Outline each blood parasite and name the species.
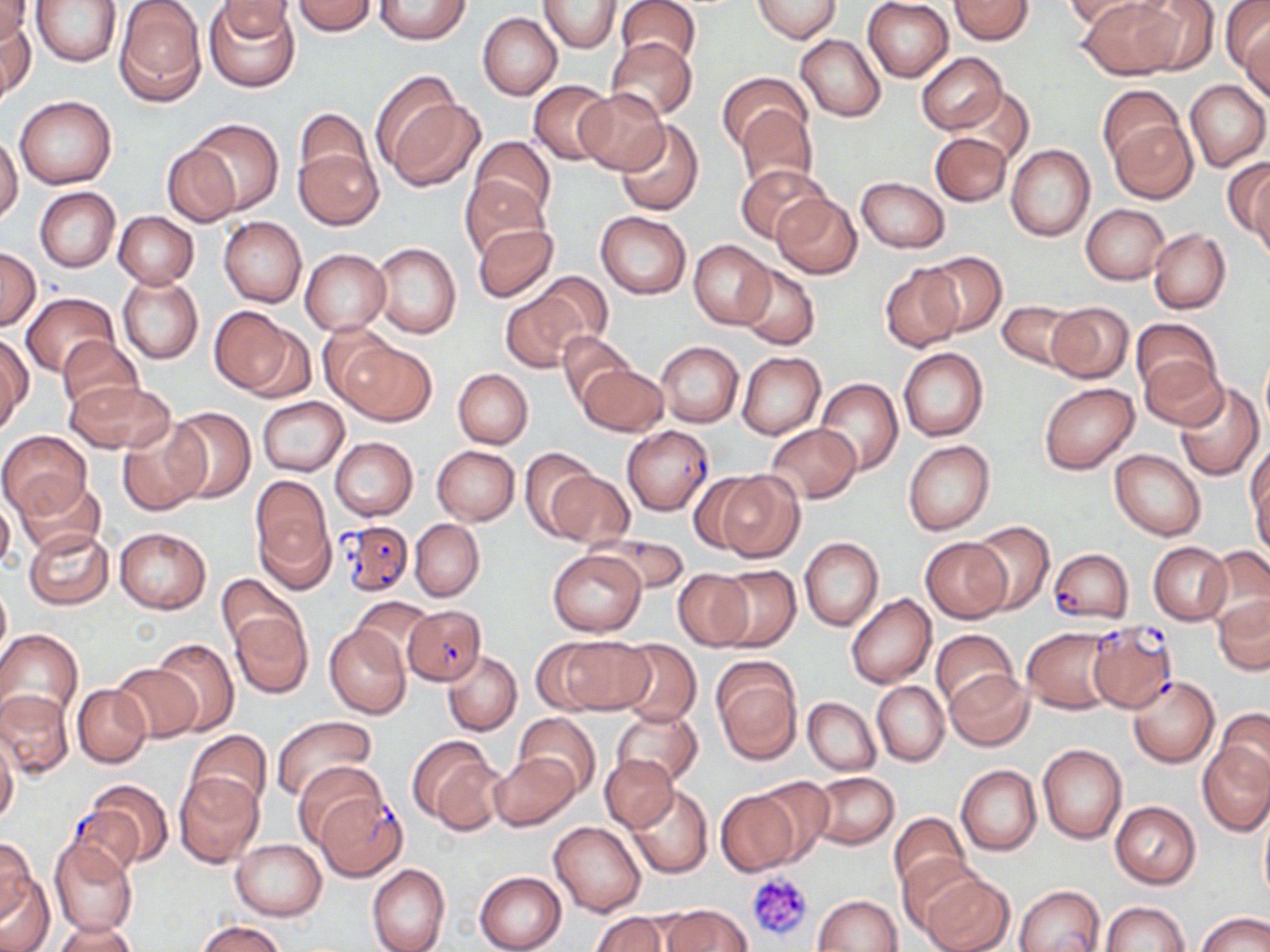

Approximate bounding boxes as named x1/y1/x2/y2 corners in pixels.
Plasmodium falciparum-infected red blood cells (subset): (x1=622, y1=426, x2=714, y2=515), (x1=341, y1=520, x2=412, y2=598), (x1=1050, y1=549, x2=1132, y2=624), (x1=403, y1=604, x2=486, y2=685), (x1=316, y1=794, x2=408, y2=880), (x1=65, y1=809, x2=148, y2=881).
No Plasmodium ovale, Plasmodium malariae, Plasmodium vivax, Babesia divergens, or Trypanosoma brucei observed.

Uninfected red blood cell locations (subset): (x1=0, y1=0, x2=32, y2=48), (x1=33, y1=0, x2=121, y2=65), (x1=215, y1=0, x2=297, y2=46), (x1=291, y1=0, x2=378, y2=36), (x1=373, y1=0, x2=472, y2=44), (x1=615, y1=0, x2=702, y2=71), (x1=752, y1=0, x2=840, y2=41), (x1=862, y1=0, x2=954, y2=82), (x1=949, y1=0, x2=1033, y2=45), (x1=1060, y1=0, x2=1152, y2=32), (x1=1075, y1=0, x2=1179, y2=79), (x1=1131, y1=0, x2=1220, y2=75), (x1=115, y1=1, x2=206, y2=105), (x1=205, y1=1, x2=299, y2=92), (x1=538, y1=1, x2=621, y2=53), (x1=1220, y1=2, x2=1270, y2=77), (x1=477, y1=12, x2=561, y2=100), (x1=2, y1=16, x2=36, y2=104), (x1=1241, y1=24, x2=1270, y2=101), (x1=795, y1=34, x2=886, y2=121), (x1=607, y1=37, x2=697, y2=121), (x1=916, y1=52, x2=1006, y2=134), (x1=370, y1=71, x2=463, y2=167), (x1=717, y1=72, x2=809, y2=152), (x1=528, y1=80, x2=617, y2=165), (x1=1185, y1=80, x2=1269, y2=171), (x1=1096, y1=85, x2=1183, y2=166), (x1=952, y1=87, x2=1032, y2=165), (x1=574, y1=88, x2=669, y2=175), (x1=388, y1=95, x2=486, y2=191), (x1=14, y1=96, x2=116, y2=189), (x1=296, y1=103, x2=373, y2=195), (x1=737, y1=104, x2=818, y2=193), (x1=188, y1=118, x2=282, y2=214), (x1=1110, y1=119, x2=1197, y2=203), (x1=615, y1=120, x2=704, y2=217), (x1=930, y1=132, x2=1011, y2=206), (x1=0, y1=135, x2=22, y2=224), (x1=471, y1=135, x2=555, y2=219), (x1=292, y1=136, x2=381, y2=230), (x1=163, y1=144, x2=240, y2=227), (x1=1005, y1=144, x2=1095, y2=241), (x1=1224, y1=159, x2=1270, y2=244), (x1=735, y1=163, x2=829, y2=244), (x1=1247, y1=164, x2=1270, y2=261), (x1=460, y1=176, x2=548, y2=259), (x1=855, y1=176, x2=949, y2=252), (x1=34, y1=186, x2=120, y2=271), (x1=771, y1=193, x2=862, y2=278), (x1=1081, y1=204, x2=1170, y2=284), (x1=595, y1=211, x2=691, y2=299), (x1=113, y1=212, x2=198, y2=288), (x1=218, y1=216, x2=306, y2=307), (x1=471, y1=222, x2=559, y2=302), (x1=1148, y1=228, x2=1231, y2=314), (x1=689, y1=241, x2=774, y2=328), (x1=371, y1=242, x2=461, y2=339), (x1=0, y1=248, x2=41, y2=330), (x1=300, y1=248, x2=391, y2=335), (x1=920, y1=251, x2=1007, y2=337), (x1=736, y1=263, x2=819, y2=350), (x1=881, y1=265, x2=962, y2=352), (x1=534, y1=271, x2=614, y2=348), (x1=118, y1=275, x2=203, y2=364), (x1=21, y1=291, x2=116, y2=378), (x1=501, y1=293, x2=583, y2=372), (x1=996, y1=300, x2=1078, y2=370), (x1=1044, y1=302, x2=1133, y2=383), (x1=210, y1=308, x2=308, y2=398), (x1=1130, y1=318, x2=1220, y2=397), (x1=319, y1=323, x2=400, y2=405), (x1=557, y1=332, x2=634, y2=407), (x1=56, y1=335, x2=142, y2=415), (x1=0, y1=337, x2=31, y2=434), (x1=339, y1=340, x2=435, y2=426), (x1=656, y1=340, x2=742, y2=428), (x1=897, y1=348, x2=988, y2=441), (x1=1135, y1=349, x2=1228, y2=432), (x1=738, y1=352, x2=825, y2=438), (x1=1260, y1=359, x2=1270, y2=433), (x1=578, y1=364, x2=667, y2=437), (x1=454, y1=369, x2=533, y2=448), (x1=64, y1=378, x2=174, y2=455), (x1=815, y1=378, x2=902, y2=475), (x1=1039, y1=382, x2=1139, y2=474), (x1=1173, y1=382, x2=1264, y2=481), (x1=257, y1=397, x2=348, y2=477), (x1=165, y1=406, x2=255, y2=502), (x1=117, y1=422, x2=208, y2=516), (x1=764, y1=423, x2=861, y2=503), (x1=0, y1=431, x2=90, y2=517), (x1=330, y1=437, x2=418, y2=520), (x1=904, y1=440, x2=994, y2=535), (x1=1247, y1=442, x2=1270, y2=541), (x1=432, y1=446, x2=519, y2=525), (x1=519, y1=447, x2=602, y2=540), (x1=1109, y1=450, x2=1205, y2=541), (x1=548, y1=468, x2=633, y2=547), (x1=710, y1=469, x2=806, y2=563), (x1=14, y1=476, x2=105, y2=557), (x1=250, y1=479, x2=333, y2=586), (x1=0, y1=494, x2=14, y2=574), (x1=409, y1=519, x2=485, y2=602), (x1=968, y1=521, x2=1055, y2=614), (x1=24, y1=527, x2=114, y2=609), (x1=115, y1=527, x2=210, y2=613), (x1=587, y1=532, x2=689, y2=596), (x1=799, y1=537, x2=883, y2=630), (x1=922, y1=538, x2=1011, y2=622), (x1=1148, y1=542, x2=1231, y2=625), (x1=1202, y1=547, x2=1270, y2=631), (x1=546, y1=549, x2=648, y2=636), (x1=713, y1=565, x2=801, y2=650), (x1=673, y1=569, x2=753, y2=650), (x1=216, y1=574, x2=303, y2=657), (x1=0, y1=578, x2=10, y2=663), (x1=846, y1=593, x2=936, y2=688), (x1=1213, y1=594, x2=1269, y2=674), (x1=351, y1=598, x2=435, y2=668), (x1=230, y1=611, x2=312, y2=698), (x1=324, y1=622, x2=410, y2=719), (x1=1022, y1=627, x2=1117, y2=714), (x1=0, y1=628, x2=84, y2=728), (x1=929, y1=628, x2=1018, y2=709), (x1=548, y1=636, x2=653, y2=715), (x1=152, y1=637, x2=238, y2=735), (x1=615, y1=639, x2=700, y2=728), (x1=442, y1=650, x2=521, y2=736), (x1=433, y1=651, x2=516, y2=814), (x1=711, y1=660, x2=801, y2=764), (x1=110, y1=661, x2=202, y2=743), (x1=945, y1=669, x2=1033, y2=751), (x1=1129, y1=677, x2=1218, y2=768), (x1=871, y1=681, x2=949, y2=766), (x1=73, y1=685, x2=152, y2=768), (x1=0, y1=688, x2=73, y2=781), (x1=803, y1=696, x2=881, y2=776), (x1=611, y1=706, x2=703, y2=789), (x1=1216, y1=709, x2=1270, y2=789), (x1=513, y1=712, x2=601, y2=800), (x1=273, y1=715, x2=376, y2=802), (x1=186, y1=730, x2=272, y2=816), (x1=0, y1=734, x2=18, y2=824), (x1=407, y1=736, x2=504, y2=832), (x1=1198, y1=742, x2=1270, y2=835), (x1=1038, y1=743, x2=1127, y2=843), (x1=489, y1=752, x2=579, y2=831), (x1=600, y1=754, x2=678, y2=832), (x1=292, y1=760, x2=385, y2=844), (x1=956, y1=765, x2=1041, y2=855), (x1=809, y1=771, x2=899, y2=849), (x1=173, y1=772, x2=265, y2=869), (x1=752, y1=776, x2=834, y2=867), (x1=86, y1=780, x2=174, y2=867), (x1=627, y1=785, x2=713, y2=878), (x1=717, y1=788, x2=803, y2=874), (x1=1109, y1=801, x2=1201, y2=888), (x1=1259, y1=807, x2=1269, y2=905), (x1=889, y1=812, x2=971, y2=900), (x1=549, y1=820, x2=646, y2=916), (x1=0, y1=835, x2=36, y2=924), (x1=49, y1=837, x2=139, y2=938), (x1=230, y1=838, x2=327, y2=920), (x1=897, y1=855, x2=985, y2=937), (x1=367, y1=864, x2=450, y2=952), (x1=0, y1=870, x2=55, y2=951), (x1=918, y1=871, x2=1015, y2=952), (x1=474, y1=872, x2=566, y2=952), (x1=1014, y1=885, x2=1104, y2=952), (x1=814, y1=894, x2=902, y2=951), (x1=1100, y1=901, x2=1190, y2=952), (x1=660, y1=904, x2=754, y2=951), (x1=591, y1=911, x2=671, y2=952), (x1=1198, y1=911, x2=1270, y2=952), (x1=198, y1=920, x2=286, y2=952), (x1=50, y1=921, x2=137, y2=951). Platelet locations: (x1=745, y1=870, x2=815, y2=943). Slide-level diagnosis: Plasmodium falciparum. Thin blood film. Captured at 1000x magnification. May-Grünwald-Giemsa stain. Single field of view. Light microscopy. Image is 1270×952 pixels.